Locate every Plasmodium parasite and identify its life-cycle stage.
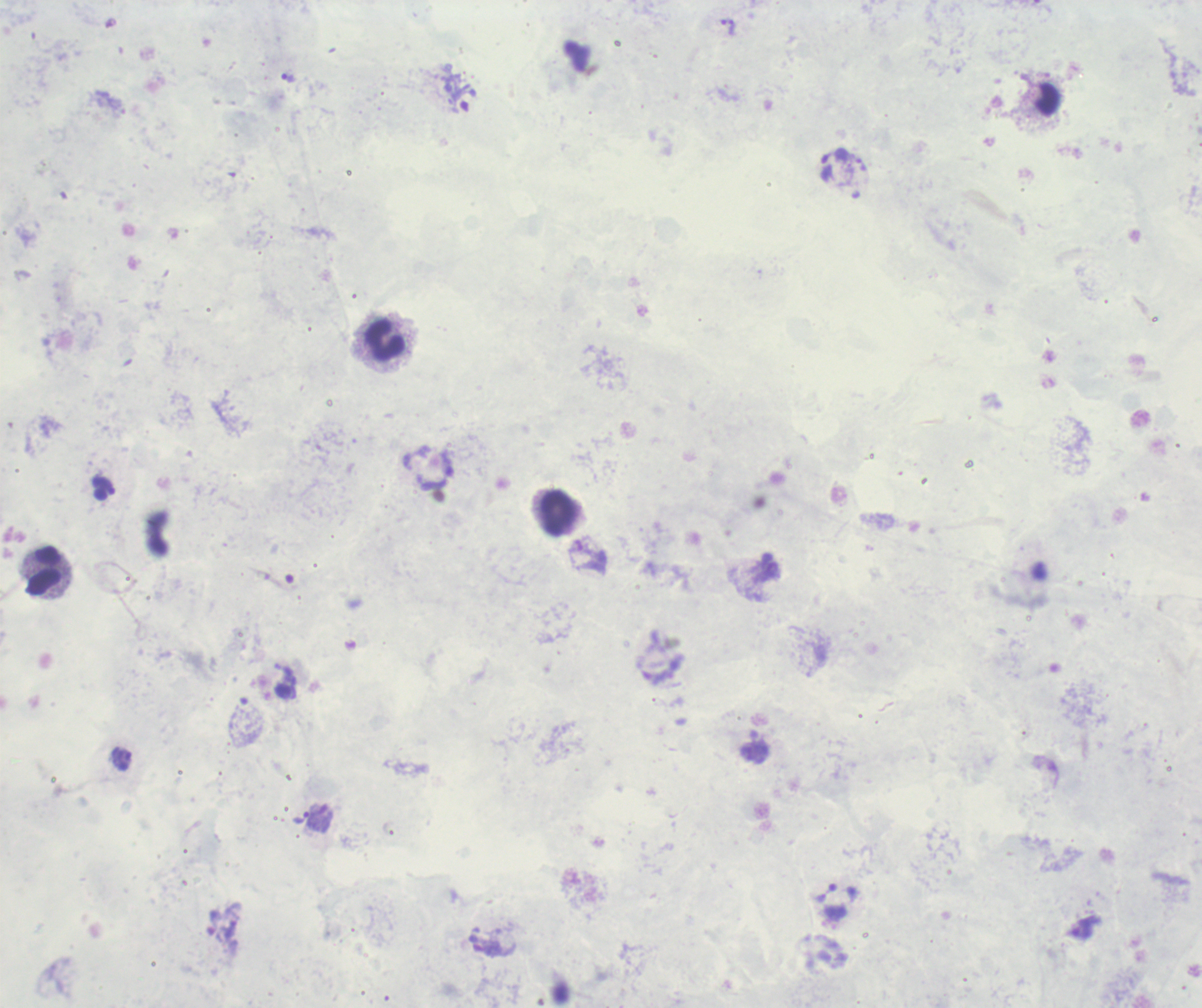
Approximate centers as {x, y} in pixels.
Trophozoites: {733, 27}, {288, 78}, {121, 758}, {311, 814}, {836, 893}, {1082, 929}.
No schizont or gametocyte forms observed.

Approximate centers as {x, y} in pixels. Leukocyte locations: {384, 342}, {558, 512}, {44, 571}. Background quality: poor. Previously used in a real diagnosis. Thick blood film. Image is 1202×1008 pixels. One field from this slide. Captured at 100x magnification. Romanowsky-stained preparation.